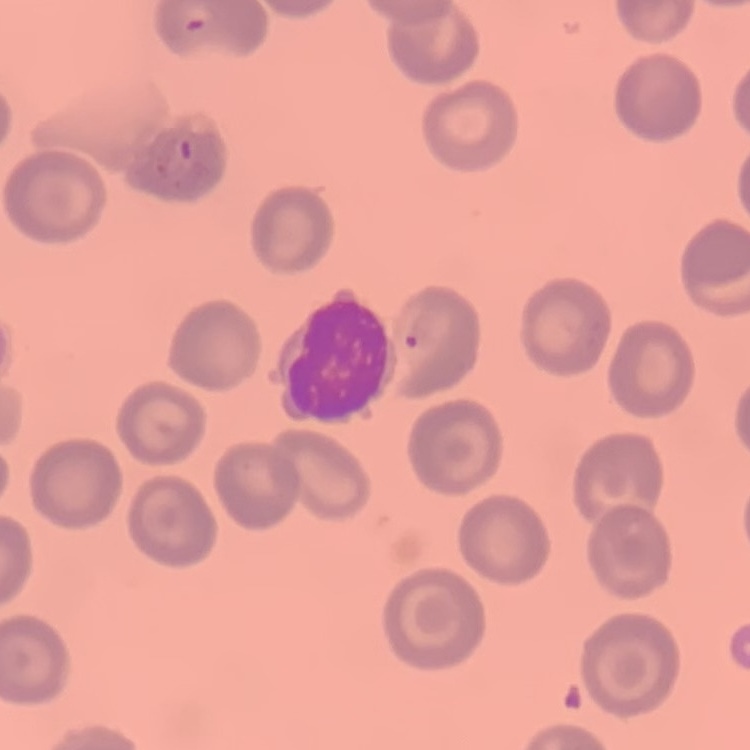 The red blood cells exhibit no rouleaux formation. Thin blood film. Stained with either Field's or Giemsa. One tile cut from a larger photomicrograph.